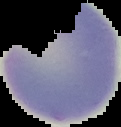

Cell region segmented out of the field of view; the surrounding area is masked to black. From a thin blood smear. Image is 121×127 pixels. Malaria status: uninfected.